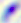

Summary:
  - Identification: Toxoplasma gondii
  - Magnification: 400x
  - Modality: photomicrograph